Locate and identify every blood parasite.
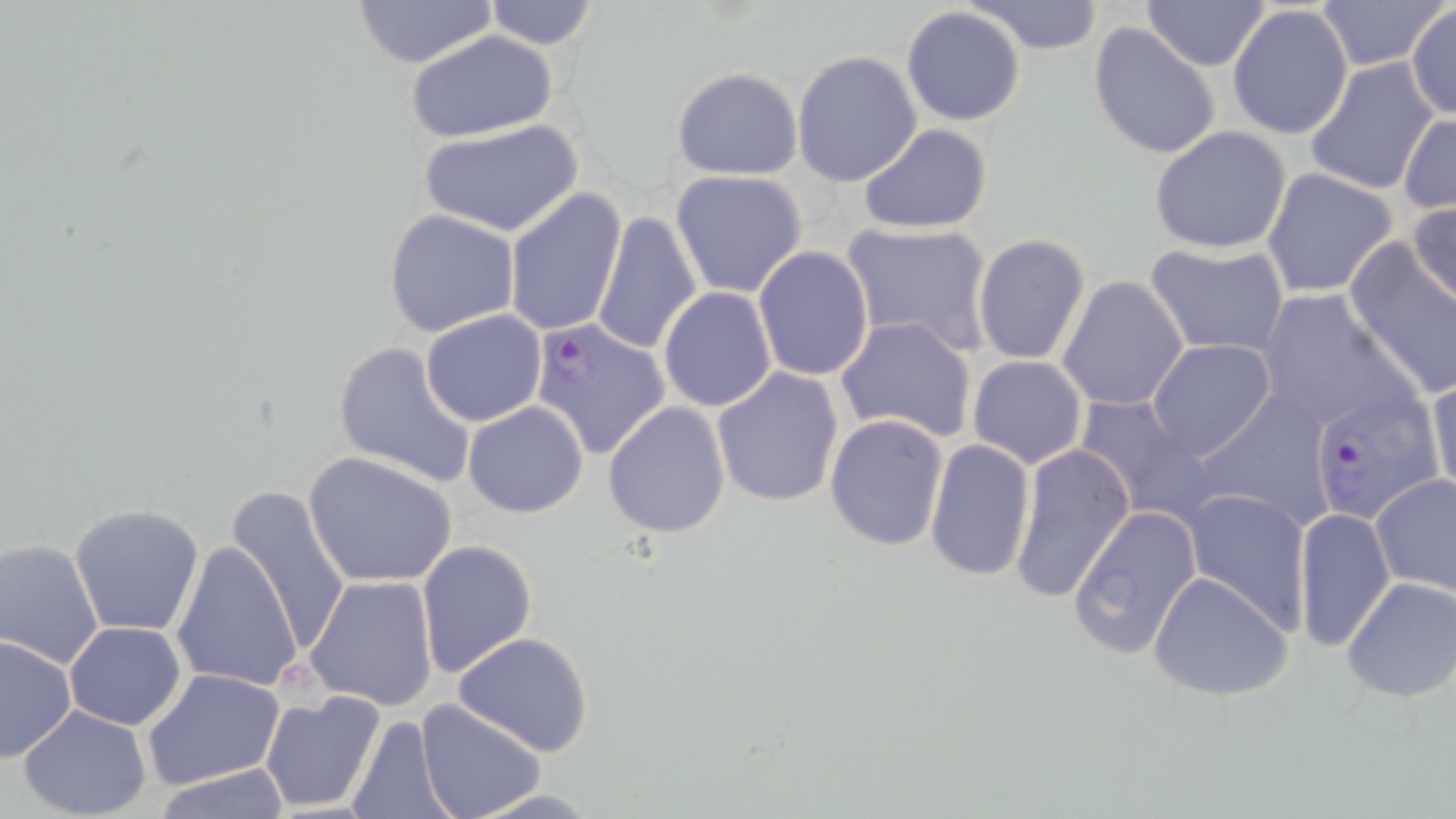
Approximate bounding boxes as (x1,y1)-(x2,y2) corner pairs in pixels.
Plasmodium falciparum-infected red blood cells: (530,316)-(672,461), (1321,394)-(1437,530).
No Plasmodium ovale, Plasmodium malariae, Plasmodium vivax, Babesia divergens, or Trypanosoma brucei observed.

Summary:
  - Uninfected red blood cell locations: (482,0)-(601,50), (964,0)-(1108,56), (1140,0)-(1273,72), (1308,0)-(1450,71), (351,1)-(500,70), (1226,3)-(1354,142), (1406,5)-(1455,120), (901,6)-(1028,127), (1088,25)-(1221,160), (407,31)-(559,143), (791,49)-(922,187), (1303,57)-(1443,196), (672,67)-(803,180), (1399,112)-(1456,215), (418,119)-(584,240), (858,124)-(993,235), (1148,126)-(1292,254), (1262,167)-(1399,298), (670,168)-(807,297), (504,186)-(627,338), (1408,198)-(1456,313), (383,208)-(521,338), (591,211)-(702,355), (840,221)-(994,355), (971,232)-(1091,365), (1343,240)-(1456,400), (1144,242)-(1290,359), (751,246)-(875,380), (1057,274)-(1190,412), (658,287)-(777,412), (1254,288)-(1420,437), (420,309)-(548,427), (833,315)-(977,445), (1146,339)-(1276,462), (331,341)-(478,489), (967,354)-(1087,468), (710,365)-(845,507), (1426,367)-(1455,507), (1190,391)-(1335,531), (1072,393)-(1215,523), (601,400)-(732,538), (463,401)-(589,518), (824,413)-(950,554), (923,437)-(1036,584), (1011,444)-(1135,603), (303,451)-(459,589), (1370,473)-(1456,598), (222,486)-(354,654), (1181,489)-(1312,631), (68,503)-(205,636), (1067,504)-(1202,660), (1292,508)-(1395,653), (1,537)-(107,670), (416,538)-(538,680), (170,541)-(305,693), (1148,569)-(1296,703), (303,574)-(439,710), (1338,576)-(1456,704), (64,621)-(188,730), (0,632)-(77,762), (453,632)-(597,757), (141,667)-(286,791), (258,691)-(385,815), (415,700)-(546,819), (18,705)-(151,818), (344,714)-(458,819), (153,763)-(295,819)
  - Slide-level diagnosis: Plasmodium falciparum
  - Magnification: 1000x
  - Modality: optical microscopy
  - Stain: May-Grünwald-Giemsa
  - Image size: 1456×819 pixels
  - Preparation: thin blood film
  - Field of view: one of a larger specimen